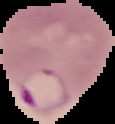
{
  "image_type": "segmented cell region with the area outside set to black",
  "preparation": "thin blood smear",
  "result": "malaria parasites detected",
  "image_size": "115×124 pixels"
}